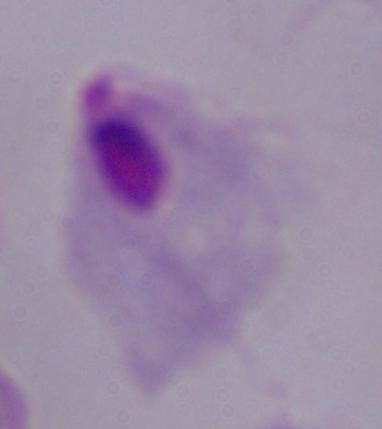
modality = photomicrograph
identification = trichomonad
magnification = 1000x